State the preparation type.
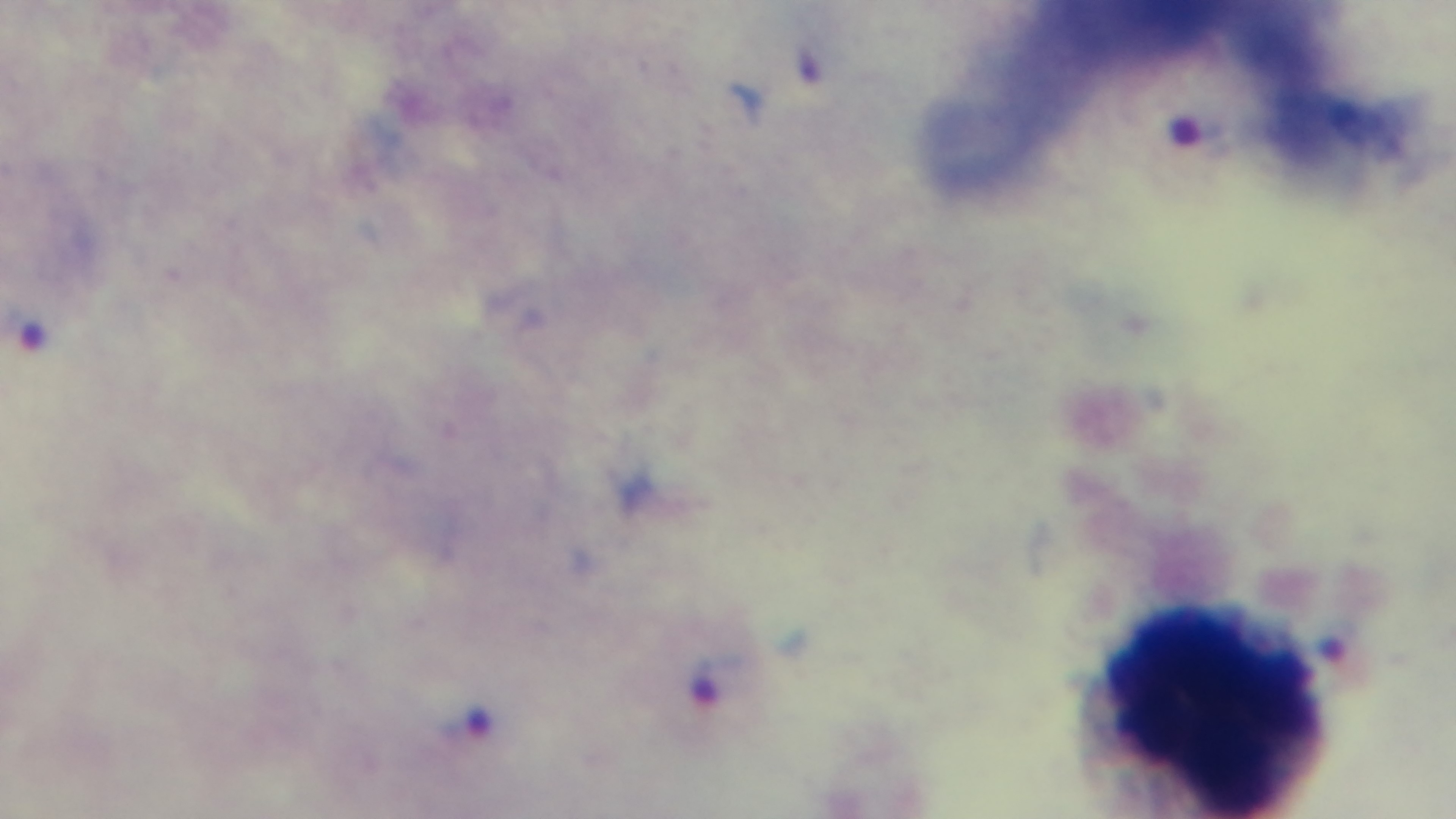

Thick.

Summary:
  - Modality: light microscopy
  - Objective: 100x oil immersion
  - Stain: Giemsa
  - Field of view: single
  - Malaria status: infected
  - Capture: mounted 4K digital camera